Assess the morphology of the erythrocytes.
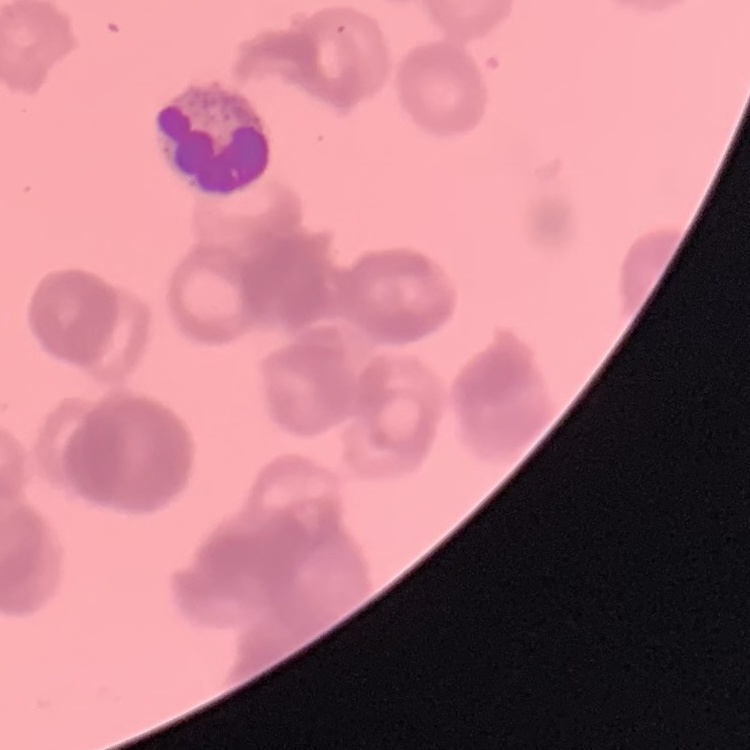

Rouleaux formation.

Field's or Giemsa stain. One tile cut from a larger photomicrograph. Thin blood film.